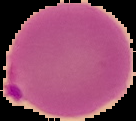

Summary:
  - Malaria status: parasitized
  - Image type: segmented cell region with the area outside set to black
  - Preparation: thin blood film
  - Image size: 136×121 pixels